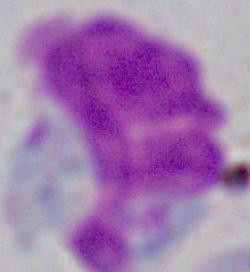

identification = leukocyte
modality = photomicrograph
magnification = 1000x